Name the blood parasite species.
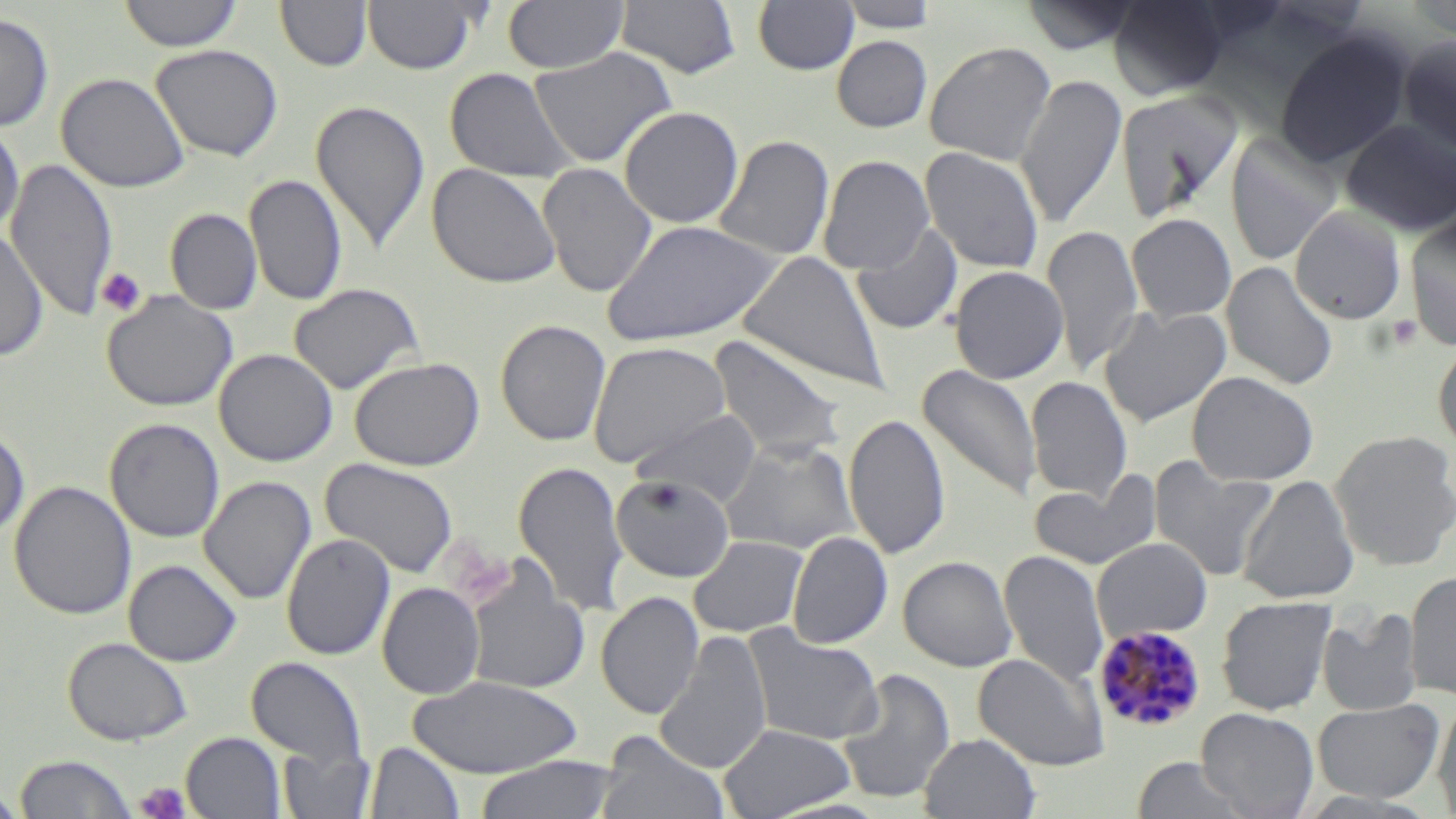

Plasmodium malariae.

Approximate bounding boxes as named x1/y1/x2/y2 corners in pixels. Uninfected red blood cell locations: (x1=118, y1=0, x2=244, y2=52), (x1=275, y1=0, x2=372, y2=71), (x1=362, y1=0, x2=481, y2=74), (x1=504, y1=0, x2=627, y2=74), (x1=617, y1=0, x2=740, y2=79), (x1=753, y1=0, x2=860, y2=75), (x1=838, y1=0, x2=940, y2=33), (x1=1108, y1=0, x2=1228, y2=99), (x1=1022, y1=1, x2=1139, y2=55), (x1=1409, y1=2, x2=1456, y2=40), (x1=0, y1=11, x2=54, y2=131), (x1=1274, y1=30, x2=1412, y2=167), (x1=832, y1=35, x2=932, y2=132), (x1=1397, y1=35, x2=1456, y2=155), (x1=924, y1=41, x2=1056, y2=165), (x1=150, y1=44, x2=283, y2=161), (x1=528, y1=47, x2=677, y2=168), (x1=444, y1=68, x2=578, y2=184), (x1=56, y1=72, x2=191, y2=193), (x1=1015, y1=74, x2=1126, y2=230), (x1=1116, y1=90, x2=1242, y2=220), (x1=310, y1=99, x2=430, y2=255), (x1=619, y1=106, x2=743, y2=228), (x1=1341, y1=119, x2=1456, y2=236), (x1=0, y1=121, x2=25, y2=238), (x1=713, y1=134, x2=834, y2=261), (x1=1225, y1=134, x2=1340, y2=266), (x1=919, y1=147, x2=1043, y2=274), (x1=818, y1=154, x2=935, y2=274), (x1=6, y1=159, x2=118, y2=321), (x1=427, y1=163, x2=562, y2=288), (x1=537, y1=163, x2=658, y2=298), (x1=244, y1=174, x2=348, y2=307), (x1=1290, y1=206, x2=1406, y2=324), (x1=165, y1=208, x2=263, y2=314), (x1=1126, y1=214, x2=1236, y2=323), (x1=1404, y1=214, x2=1456, y2=350), (x1=601, y1=219, x2=782, y2=347), (x1=851, y1=223, x2=963, y2=335), (x1=1042, y1=225, x2=1143, y2=375), (x1=0, y1=230, x2=48, y2=362), (x1=739, y1=251, x2=890, y2=395), (x1=1222, y1=261, x2=1338, y2=390), (x1=949, y1=265, x2=1068, y2=384), (x1=288, y1=283, x2=424, y2=395), (x1=101, y1=290, x2=238, y2=412), (x1=1099, y1=305, x2=1231, y2=427), (x1=495, y1=319, x2=611, y2=446), (x1=708, y1=334, x2=845, y2=462), (x1=1432, y1=338, x2=1456, y2=453), (x1=587, y1=340, x2=732, y2=468), (x1=213, y1=348, x2=338, y2=467), (x1=349, y1=357, x2=485, y2=471), (x1=917, y1=364, x2=1042, y2=502), (x1=1187, y1=371, x2=1319, y2=485), (x1=1026, y1=375, x2=1133, y2=502), (x1=630, y1=409, x2=763, y2=506), (x1=843, y1=413, x2=950, y2=559), (x1=104, y1=418, x2=225, y2=543), (x1=0, y1=424, x2=30, y2=541), (x1=1330, y1=430, x2=1456, y2=571), (x1=720, y1=438, x2=859, y2=554), (x1=320, y1=457, x2=459, y2=579), (x1=1148, y1=457, x2=1277, y2=582), (x1=513, y1=459, x2=630, y2=618), (x1=1030, y1=472, x2=1161, y2=571), (x1=611, y1=474, x2=735, y2=583), (x1=1238, y1=475, x2=1359, y2=603), (x1=198, y1=476, x2=317, y2=605), (x1=9, y1=480, x2=137, y2=620), (x1=787, y1=531, x2=893, y2=649), (x1=281, y1=534, x2=395, y2=660), (x1=688, y1=535, x2=809, y2=638), (x1=1092, y1=537, x2=1212, y2=642), (x1=1000, y1=550, x2=1108, y2=688), (x1=897, y1=556, x2=1017, y2=672), (x1=123, y1=559, x2=242, y2=667), (x1=463, y1=560, x2=591, y2=695), (x1=1404, y1=571, x2=1456, y2=700), (x1=377, y1=582, x2=485, y2=699), (x1=596, y1=591, x2=704, y2=719), (x1=1217, y1=596, x2=1337, y2=716), (x1=1317, y1=608, x2=1423, y2=717), (x1=743, y1=626, x2=884, y2=745), (x1=654, y1=630, x2=773, y2=776), (x1=62, y1=636, x2=193, y2=746), (x1=973, y1=652, x2=1109, y2=771), (x1=246, y1=656, x2=367, y2=773), (x1=836, y1=668, x2=956, y2=805), (x1=408, y1=674, x2=584, y2=778), (x1=1312, y1=698, x2=1444, y2=804), (x1=1432, y1=701, x2=1456, y2=817), (x1=1196, y1=707, x2=1318, y2=819), (x1=718, y1=723, x2=856, y2=818), (x1=181, y1=732, x2=286, y2=819), (x1=596, y1=733, x2=727, y2=819), (x1=919, y1=733, x2=1039, y2=819), (x1=364, y1=741, x2=464, y2=819), (x1=278, y1=742, x2=375, y2=819), (x1=14, y1=754, x2=138, y2=818), (x1=472, y1=756, x2=622, y2=819), (x1=1131, y1=758, x2=1250, y2=819), (x1=0, y1=783, x2=25, y2=818). Platelet locations: (x1=96, y1=267, x2=147, y2=318), (x1=1387, y1=316, x2=1423, y2=349), (x1=134, y1=782, x2=192, y2=819). Plasmodium malariae-infected red blood cell locations: (x1=1092, y1=625, x2=1208, y2=734). Thin blood smear. May-Grünwald-Giemsa-stained preparation. Image is 1456×819 pixels. Single field of view. 1000x magnification. Optical microscopy.